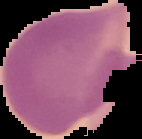
{
  "preparation": "thin blood film",
  "image_type": "cell region segmented out of the field of view; surrounding area masked to black",
  "image_size": "142×139 pixels",
  "malaria_status": "uninfected"
}